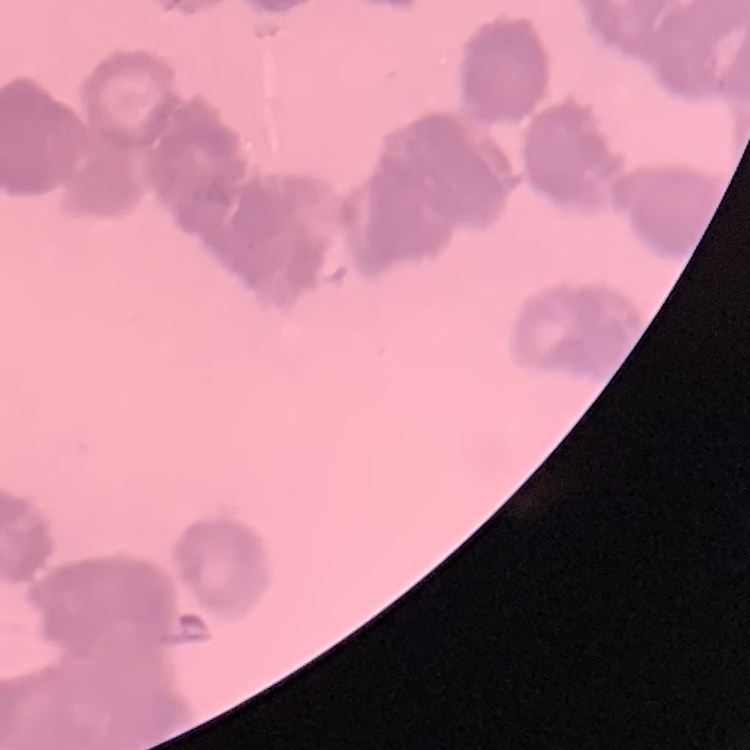
erythrocyte morphology = rouleaux formation
image type = one tile cut from a larger photomicrograph
preparation = thin blood smear
stain = Field's or Giemsa